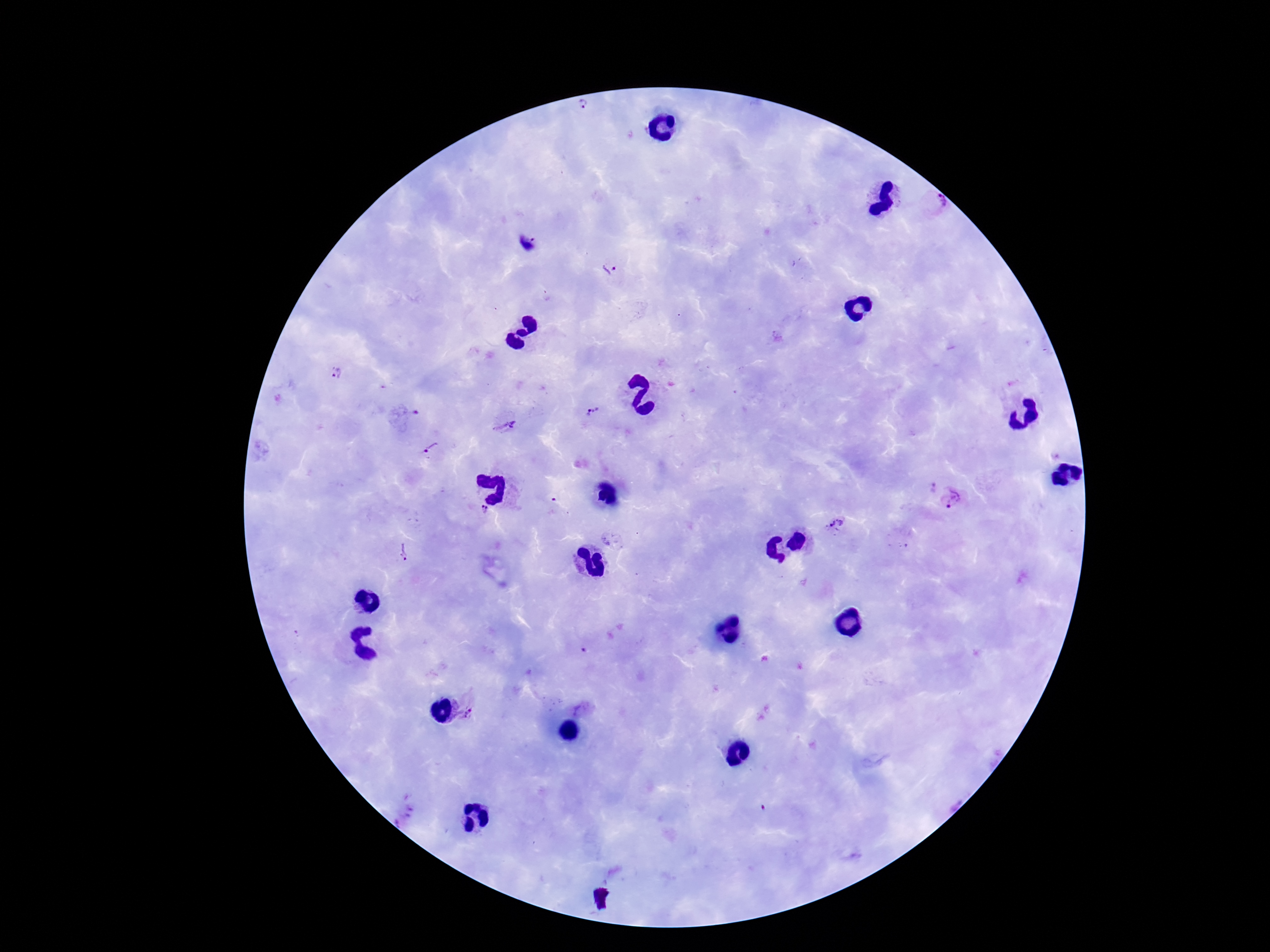

Approximate centers as [x, y] in pixels.
Summary:
  - Plasmodium parasite locations: [584, 108], [937, 201], [528, 244], [610, 270], [336, 373], [592, 412], [409, 414], [505, 428], [432, 448], [930, 489], [954, 497], [483, 512], [843, 521], [830, 523], [403, 552], [471, 714], [403, 813]
  - Magnification: 100x
  - Field of view: one from this slide
  - Preparation: thick blood film
  - Image size: 1270×952 pixels
  - Patient malaria status: infected
  - Stain: Giemsa
  - Capture: smartphone camera through the microscope eyepiece